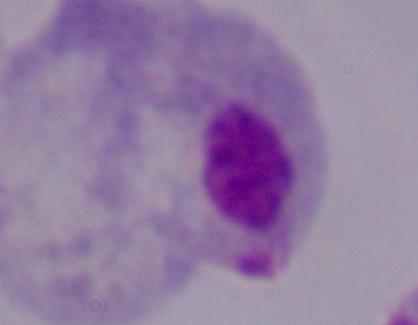

Micrograph. A trichomonad is shown. Captured at 1000x magnification.